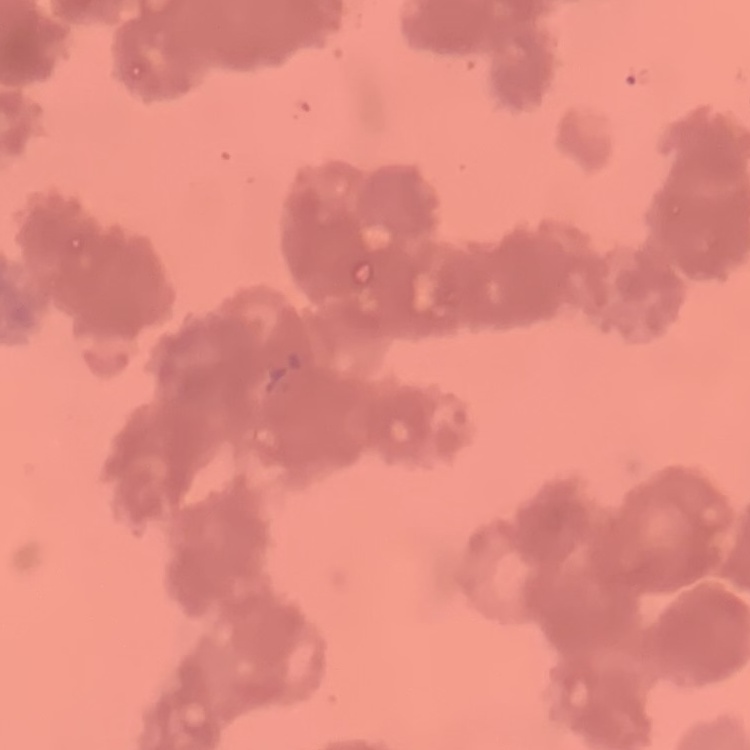

erythrocyte morphology = rouleaux formation
image type = one tile cut from a larger photomicrograph
preparation = thin peripheral smear
stain = Field's or Giemsa